Identify the blood parasite species.
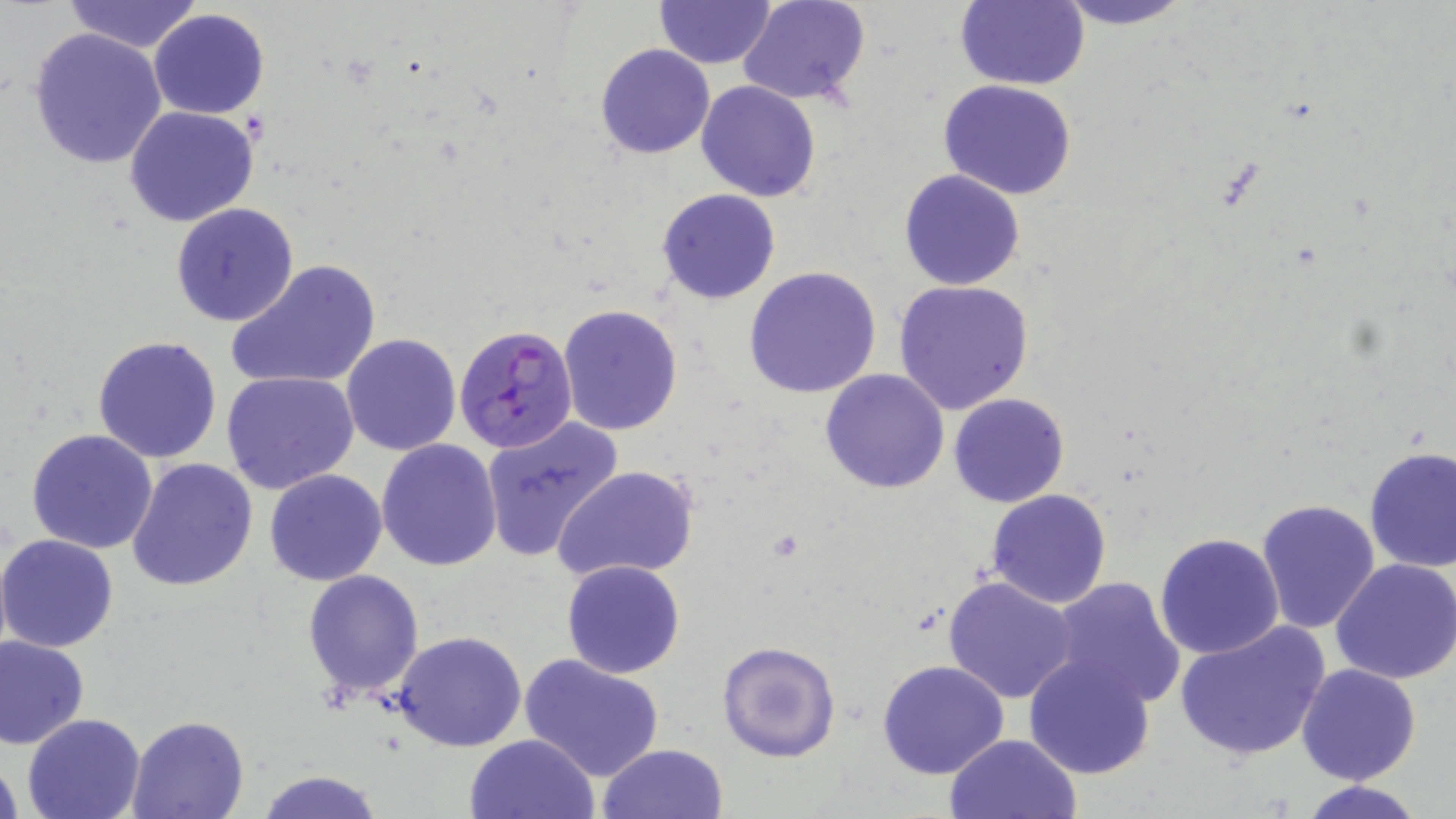

Plasmodium falciparum.

Approximate bounding boxes as (x1,y1)-(x2,y2) corner pairs in pixels. Uninfected red blood cell locations: (63,0)-(203,53), (738,0)-(873,107), (954,0)-(1089,90), (1051,0)-(1197,28), (654,1)-(776,68), (149,9)-(270,120), (27,26)-(168,169), (594,44)-(715,160), (938,80)-(1078,201), (696,81)-(822,202), (123,105)-(259,226), (899,168)-(1025,290), (657,189)-(782,305), (170,202)-(299,327), (228,259)-(380,394), (743,266)-(882,398), (892,279)-(1035,414), (556,304)-(683,436), (341,333)-(463,456), (92,335)-(223,465), (820,369)-(951,495), (222,371)-(360,496), (950,392)-(1070,509), (480,419)-(624,563), (27,427)-(159,553), (377,440)-(503,571), (1362,446)-(1456,573), (126,457)-(259,593), (553,464)-(700,585), (263,470)-(388,587), (985,488)-(1113,609), (1256,498)-(1380,634), (1155,532)-(1286,660), (0,534)-(119,654), (1330,556)-(1456,684), (561,559)-(686,679), (302,569)-(424,698), (944,576)-(1078,703), (1049,577)-(1185,707), (1172,620)-(1331,762), (393,632)-(528,751), (0,635)-(89,749), (717,640)-(840,762), (520,652)-(665,782), (1023,654)-(1156,780), (877,659)-(1010,778), (1296,663)-(1422,785), (21,712)-(145,819), (126,714)-(250,818), (464,734)-(599,819), (943,734)-(1083,819), (598,743)-(728,819), (0,749)-(24,818), (252,769)-(385,819), (1296,778)-(1429,818). Plasmodium falciparum-infected red blood cell locations: (454,323)-(578,454). Captured at 1000x magnification. May-Grünwald-Giemsa stain. Image is 1456×819 pixels. One field of a larger specimen. Thin blood smear. Optical microscopy.